Identify the blood parasite species.
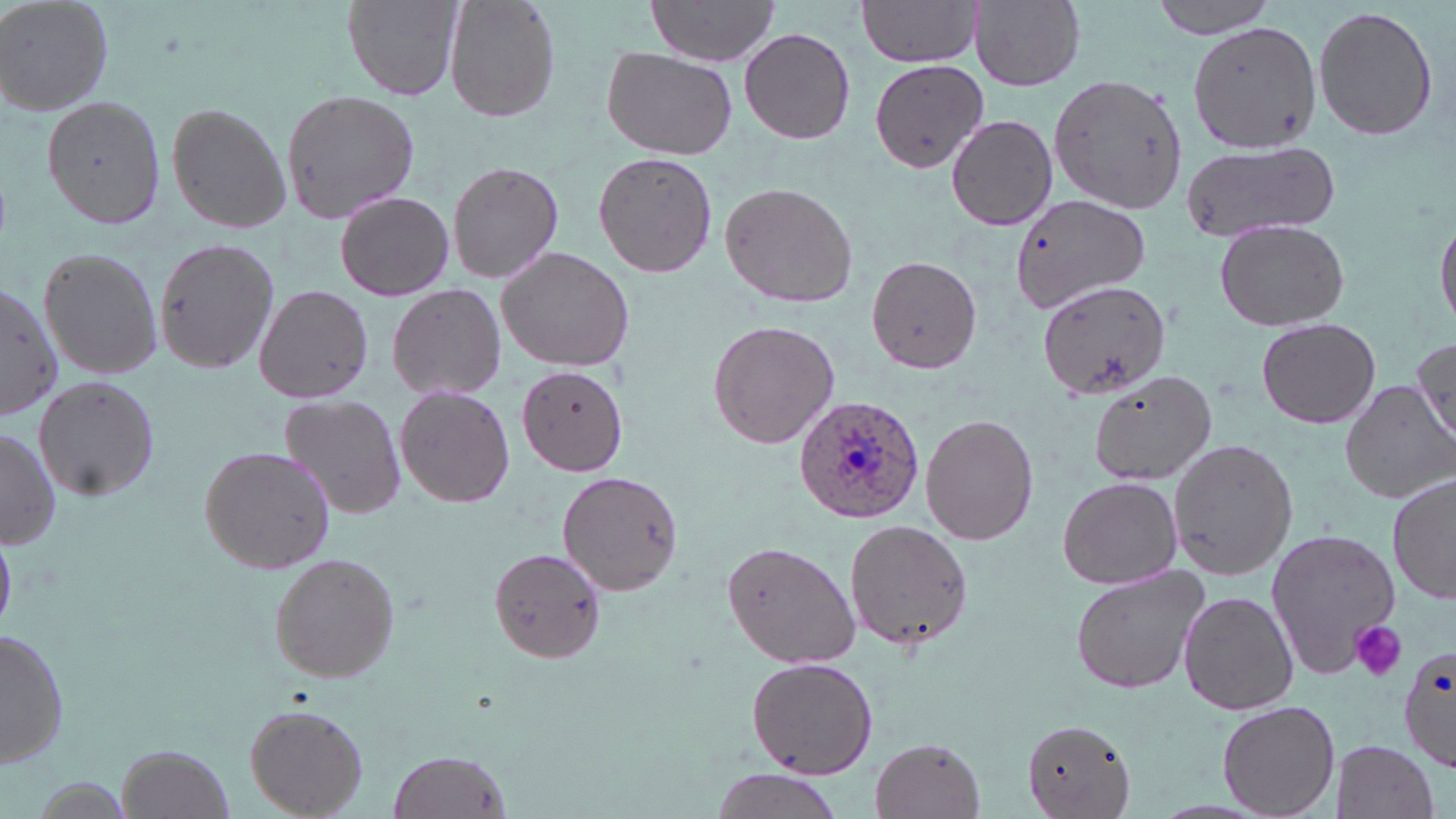
Plasmodium ovale.

Summary:
  - Coordinate format: approximate bounding boxes as named x1/y1/x2/y2 corners in pixels
  - Platelet locations: (x1=1350, y1=621, x2=1407, y2=681)
  - Plasmodium ovale-infected red blood cell locations: (x1=795, y1=395, x2=927, y2=524)
  - Uninfected red blood cell locations: (x1=0, y1=0, x2=116, y2=116), (x1=342, y1=0, x2=462, y2=102), (x1=444, y1=0, x2=561, y2=124), (x1=646, y1=0, x2=781, y2=66), (x1=968, y1=0, x2=1086, y2=90), (x1=1152, y1=0, x2=1283, y2=40), (x1=855, y1=1, x2=985, y2=67), (x1=1313, y1=4, x2=1439, y2=142), (x1=1188, y1=19, x2=1319, y2=151), (x1=739, y1=26, x2=857, y2=145), (x1=600, y1=46, x2=736, y2=161), (x1=869, y1=60, x2=988, y2=172), (x1=1047, y1=73, x2=1190, y2=217), (x1=280, y1=89, x2=417, y2=219), (x1=41, y1=92, x2=167, y2=231), (x1=164, y1=100, x2=292, y2=236), (x1=946, y1=113, x2=1059, y2=233), (x1=1180, y1=142, x2=1339, y2=245), (x1=593, y1=150, x2=718, y2=278), (x1=446, y1=160, x2=564, y2=284), (x1=719, y1=181, x2=857, y2=310), (x1=334, y1=190, x2=455, y2=302), (x1=1008, y1=193, x2=1150, y2=315), (x1=1435, y1=211, x2=1456, y2=338), (x1=1213, y1=218, x2=1351, y2=333), (x1=152, y1=235, x2=280, y2=375), (x1=494, y1=245, x2=636, y2=374), (x1=37, y1=246, x2=162, y2=380), (x1=865, y1=253, x2=984, y2=375), (x1=1037, y1=280, x2=1171, y2=400), (x1=0, y1=282, x2=62, y2=420), (x1=385, y1=282, x2=508, y2=401), (x1=254, y1=285, x2=373, y2=404), (x1=1255, y1=317, x2=1382, y2=427), (x1=706, y1=318, x2=841, y2=450), (x1=1411, y1=338, x2=1454, y2=446), (x1=516, y1=366, x2=629, y2=477), (x1=1089, y1=368, x2=1220, y2=484), (x1=34, y1=377, x2=160, y2=501), (x1=1341, y1=380, x2=1455, y2=505), (x1=395, y1=385, x2=516, y2=508), (x1=277, y1=393, x2=407, y2=519), (x1=922, y1=414, x2=1039, y2=545), (x1=0, y1=425, x2=59, y2=553), (x1=1166, y1=438, x2=1300, y2=580), (x1=198, y1=445, x2=337, y2=574), (x1=558, y1=470, x2=687, y2=596), (x1=1056, y1=474, x2=1184, y2=590), (x1=1387, y1=474, x2=1455, y2=609), (x1=843, y1=520, x2=975, y2=653), (x1=1264, y1=526, x2=1401, y2=678), (x1=722, y1=539, x2=859, y2=671), (x1=489, y1=546, x2=609, y2=663), (x1=267, y1=552, x2=401, y2=684), (x1=1067, y1=566, x2=1209, y2=697), (x1=1176, y1=590, x2=1301, y2=717), (x1=1, y1=626, x2=74, y2=768), (x1=1399, y1=643, x2=1455, y2=770), (x1=744, y1=656, x2=879, y2=780), (x1=1217, y1=700, x2=1341, y2=819), (x1=241, y1=702, x2=371, y2=817), (x1=1022, y1=719, x2=1135, y2=817), (x1=869, y1=735, x2=988, y2=818), (x1=1330, y1=738, x2=1442, y2=819), (x1=119, y1=744, x2=231, y2=818), (x1=386, y1=748, x2=511, y2=819), (x1=706, y1=771, x2=845, y2=819)
  - Image size: 1456×819 pixels
  - Stain: May-Grünwald-Giemsa
  - Modality: light microscopy
  - Magnification: 1000x
  - Preparation: thin blood film
  - Field of view: single